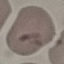

malaria_status: uninfected
capture: smartphone through the microscope eyepiece
image_type: cell patch, automatically extracted from a larger field of view and resized to 64 × 64 pixels
preparation: thin blood film
stain: Giemsa